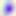

Summary:
  - Magnification: 400x
  - Identification: Toxoplasma gondii
  - Modality: micrograph